Locate every uninfected red blood cell.
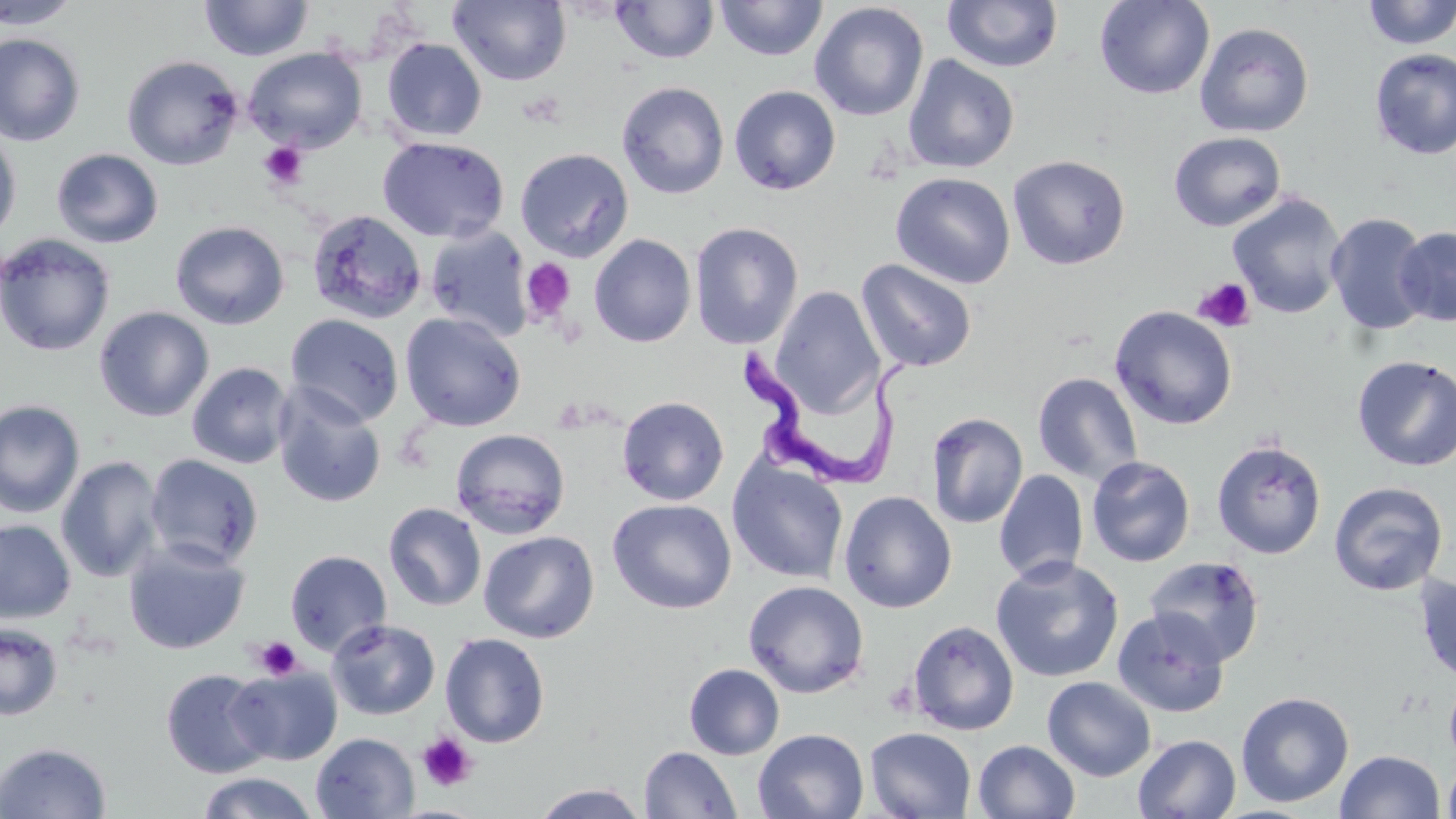
Approximate bounding boxes as named x1/y1/x2/y2 corners in pixels.
Uninfected red blood cells: (x1=0, y1=0, x2=81, y2=29), (x1=448, y1=0, x2=572, y2=86), (x1=715, y1=0, x2=828, y2=61), (x1=1093, y1=0, x2=1215, y2=100), (x1=199, y1=1, x2=314, y2=61), (x1=610, y1=1, x2=720, y2=64), (x1=942, y1=1, x2=1063, y2=73), (x1=1361, y1=1, x2=1456, y2=50), (x1=809, y1=3, x2=929, y2=121), (x1=1194, y1=22, x2=1314, y2=138), (x1=0, y1=33, x2=86, y2=146), (x1=381, y1=38, x2=487, y2=142), (x1=243, y1=47, x2=367, y2=153), (x1=1370, y1=48, x2=1456, y2=159), (x1=121, y1=54, x2=245, y2=170), (x1=902, y1=54, x2=1019, y2=174), (x1=616, y1=81, x2=729, y2=199), (x1=729, y1=85, x2=841, y2=195), (x1=0, y1=126, x2=22, y2=245), (x1=1169, y1=132, x2=1286, y2=232), (x1=377, y1=137, x2=510, y2=243), (x1=51, y1=148, x2=163, y2=248), (x1=515, y1=148, x2=633, y2=262), (x1=1008, y1=154, x2=1131, y2=269), (x1=890, y1=172, x2=1015, y2=289), (x1=1227, y1=192, x2=1347, y2=319), (x1=307, y1=209, x2=427, y2=325), (x1=1325, y1=212, x2=1432, y2=337), (x1=170, y1=221, x2=290, y2=329), (x1=690, y1=222, x2=804, y2=350), (x1=425, y1=225, x2=533, y2=342), (x1=1394, y1=226, x2=1456, y2=326), (x1=0, y1=233, x2=116, y2=357), (x1=589, y1=233, x2=696, y2=347), (x1=856, y1=259, x2=977, y2=373), (x1=769, y1=286, x2=884, y2=416), (x1=1109, y1=305, x2=1238, y2=430), (x1=94, y1=306, x2=214, y2=422), (x1=286, y1=313, x2=404, y2=426), (x1=400, y1=313, x2=525, y2=431), (x1=1352, y1=354, x2=1456, y2=472), (x1=186, y1=362, x2=295, y2=469), (x1=1032, y1=372, x2=1143, y2=486), (x1=273, y1=386, x2=388, y2=509), (x1=617, y1=396, x2=729, y2=505), (x1=0, y1=400, x2=85, y2=518), (x1=926, y1=412, x2=1028, y2=528), (x1=450, y1=428, x2=571, y2=540), (x1=1211, y1=438, x2=1327, y2=559), (x1=144, y1=453, x2=264, y2=570), (x1=56, y1=456, x2=164, y2=583), (x1=1086, y1=456, x2=1196, y2=567), (x1=727, y1=457, x2=849, y2=583), (x1=994, y1=469, x2=1088, y2=584), (x1=729, y1=474, x2=959, y2=593), (x1=1328, y1=481, x2=1449, y2=597), (x1=838, y1=490, x2=957, y2=613), (x1=608, y1=498, x2=737, y2=614), (x1=383, y1=502, x2=487, y2=612), (x1=0, y1=519, x2=76, y2=624), (x1=479, y1=530, x2=599, y2=643), (x1=122, y1=538, x2=250, y2=655), (x1=285, y1=549, x2=392, y2=656), (x1=990, y1=555, x2=1125, y2=683), (x1=1144, y1=556, x2=1266, y2=666), (x1=1414, y1=573, x2=1456, y2=686), (x1=743, y1=581, x2=870, y2=698), (x1=1112, y1=608, x2=1230, y2=718), (x1=327, y1=618, x2=440, y2=720), (x1=907, y1=619, x2=1020, y2=735), (x1=0, y1=621, x2=63, y2=721), (x1=440, y1=633, x2=551, y2=747), (x1=684, y1=663, x2=785, y2=760), (x1=228, y1=665, x2=342, y2=765), (x1=160, y1=669, x2=274, y2=778), (x1=1444, y1=673, x2=1456, y2=772), (x1=1042, y1=676, x2=1156, y2=781), (x1=1235, y1=691, x2=1355, y2=808), (x1=864, y1=727, x2=977, y2=818), (x1=753, y1=728, x2=869, y2=818), (x1=311, y1=732, x2=419, y2=818), (x1=1133, y1=734, x2=1241, y2=819), (x1=972, y1=739, x2=1080, y2=819), (x1=0, y1=742, x2=112, y2=819), (x1=639, y1=746, x2=742, y2=818), (x1=1334, y1=749, x2=1446, y2=819), (x1=1441, y1=755, x2=1456, y2=819), (x1=197, y1=771, x2=319, y2=819), (x1=531, y1=783, x2=651, y2=818).

Summary:
  - Platelet locations: (x1=258, y1=141, x2=309, y2=189), (x1=520, y1=258, x2=577, y2=324), (x1=1193, y1=277, x2=1256, y2=333), (x1=254, y1=636, x2=302, y2=680), (x1=417, y1=732, x2=478, y2=792)
  - Trypanosoma brucei locations: (x1=740, y1=334, x2=908, y2=491)
  - Slide-level diagnosis: Trypanosoma brucei
  - Modality: optical microscopy
  - Preparation: thin blood film
  - Magnification: 1000x
  - Stain: May-Grünwald-Giemsa
  - Field of view: one of a larger specimen
  - Image size: 1456×819 pixels